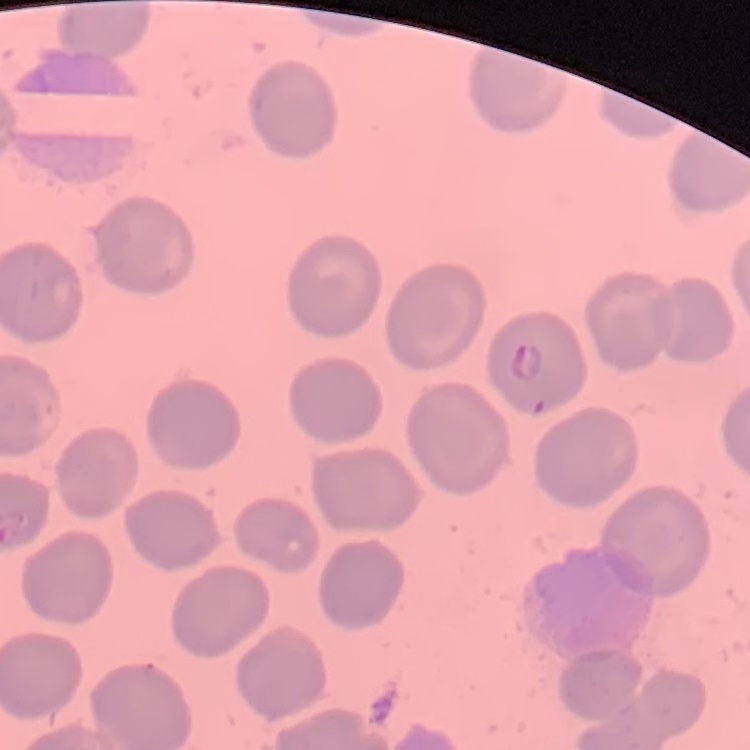
The red blood cells show no rouleaux formation. Stained with either Field's or Giemsa. Square crop of a larger photomicrograph. Thin peripheral smear.